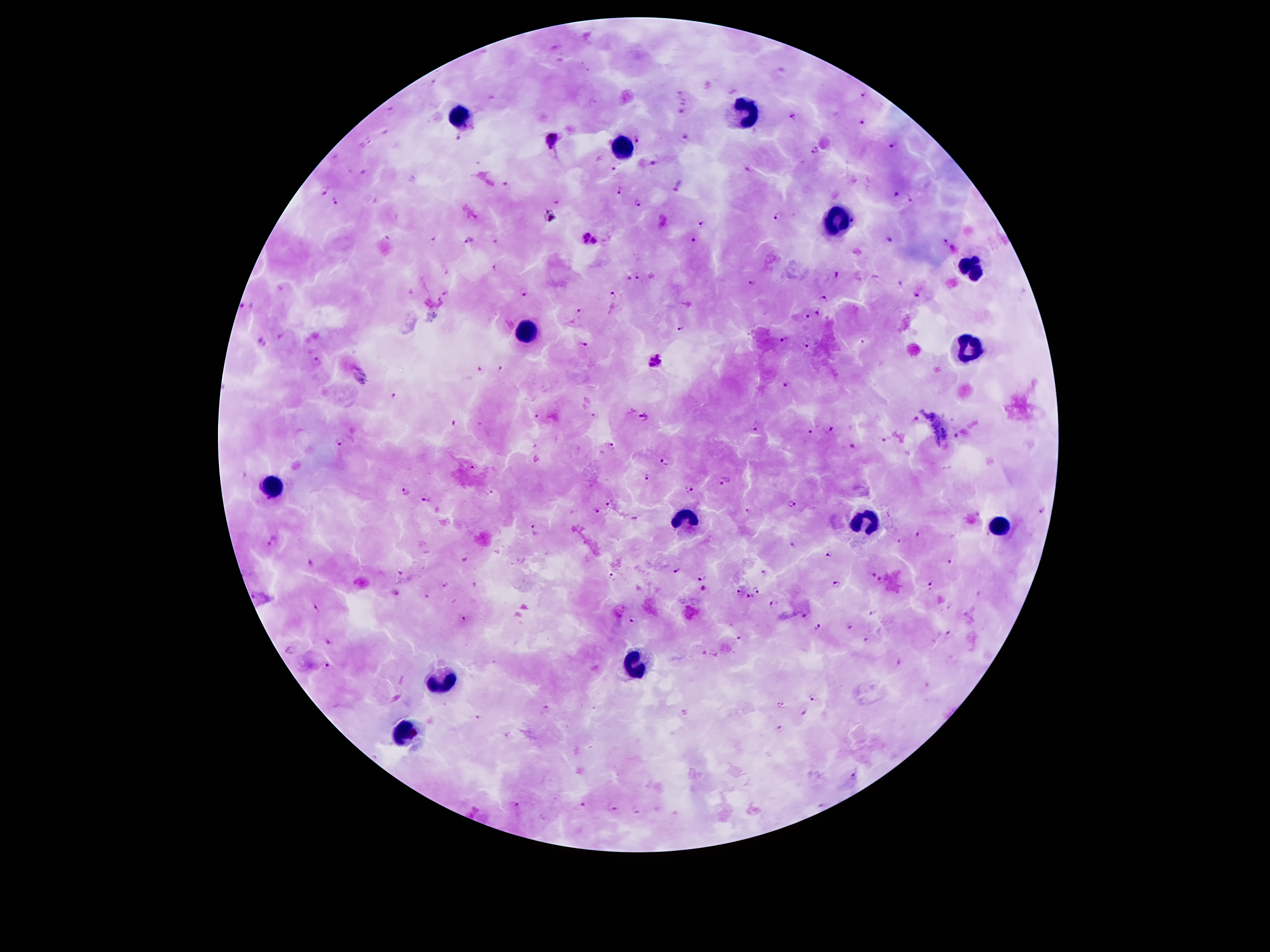

stain: Giemsa
capture: smartphone camera through the microscope eyepiece
malaria_parasite_locations: 'approximate centers as [x, y] in pixels: [782, 70], [732, 91], [681, 92], [860, 96], [684, 103], [391, 111], [681, 113], [792, 117], [860, 121], [384, 132], [553, 138], [637, 139], [686, 139], [459, 140], [370, 141], [892, 146], [361, 148], [814, 152], [335, 157], [651, 163], [746, 169], [367, 171], [614, 171], [413, 180], [506, 187], [678, 188], [324, 190], [618, 191], [895, 195], [912, 201], [556, 202], [336, 203], [637, 204], [551, 216], [776, 216], [702, 224], [888, 238], [469, 239], [591, 239], [692, 239], [943, 240], [432, 241], [496, 243], [954, 248], [496, 268], [446, 273], [836, 275], [639, 279], [627, 280], [899, 281], [752, 283], [523, 292], [446, 293], [613, 294], [916, 295], [823, 299], [247, 306], [578, 310], [818, 314], [806, 318], [679, 328], [783, 341], [263, 342], [581, 344], [807, 345], [315, 360], [655, 361], [479, 370], [501, 370], [787, 384], [392, 398], [537, 415], [595, 416], [643, 418], [915, 419], [452, 423], [755, 426], [828, 429], [809, 430], [957, 437], [886, 441], [340, 442], [611, 445], [855, 449], [664, 462], [475, 468], [243, 475], [646, 477], [725, 482], [688, 489], [489, 490], [403, 492], [427, 497], [792, 504], [607, 505], [595, 511], [747, 512], [1042, 512], [535, 531], [920, 533], [271, 541], [901, 542], [794, 548], [828, 554], [949, 563], [311, 564], [399, 571], [677, 571], [765, 574], [871, 574], [702, 577], [613, 578], [883, 578], [837, 583], [475, 584], [448, 585], [927, 588], [703, 590], [758, 590], [396, 592], [739, 592], [255, 595], [426, 595], [751, 596], [773, 603], [315, 606], [951, 606], [803, 616], [465, 619], [634, 620], [820, 626], [849, 626], [949, 636], [739, 638], [328, 641], [866, 641], [290, 650], [897, 662], [327, 665], [815, 696], [780, 707], [545, 709], [802, 713], [476, 717], [780, 730], [851, 773], [515, 804], [584, 804], [821, 806], [614, 811], [636, 811]'
patient_malaria_status: infected with Plasmodium falciparum
field_of_view: single
magnification: 100x
preparation: thick blood smear
leukocyte_locations: 'approximate centers as [x, y] in pixels: [748, 113], [459, 116], [624, 146], [837, 223], [970, 268], [529, 326], [967, 349], [272, 487], [687, 517], [867, 520], [998, 527], [634, 664], [442, 679], [405, 732]'
image_size: 1270×952 pixels